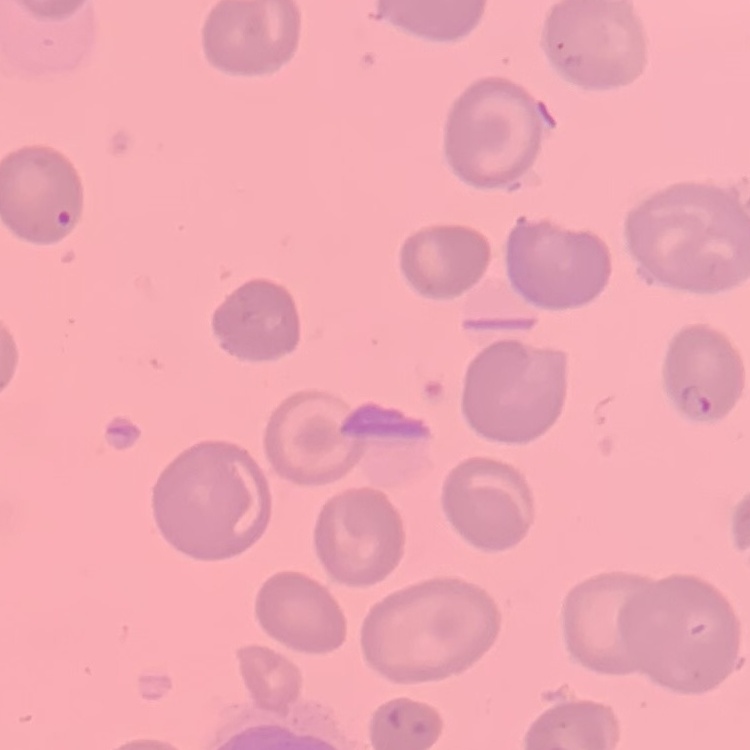

The red blood cells show no rouleaux formation. Field's or Giemsa stain. Thin peripheral smear. One tile cut from a larger photomicrograph.